Assess this cell for malaria.
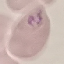

Parasitized.

Summary:
  - Preparation: thin smear
  - Capture: smartphone camera at the microscope eyepiece
  - Image type: automatically extracted cell patch, resized to 64 × 64 pixels
  - Stain: Giemsa